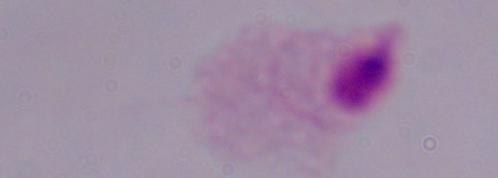
Micrograph. Captured at 1000x magnification. A trichomonad is seen.